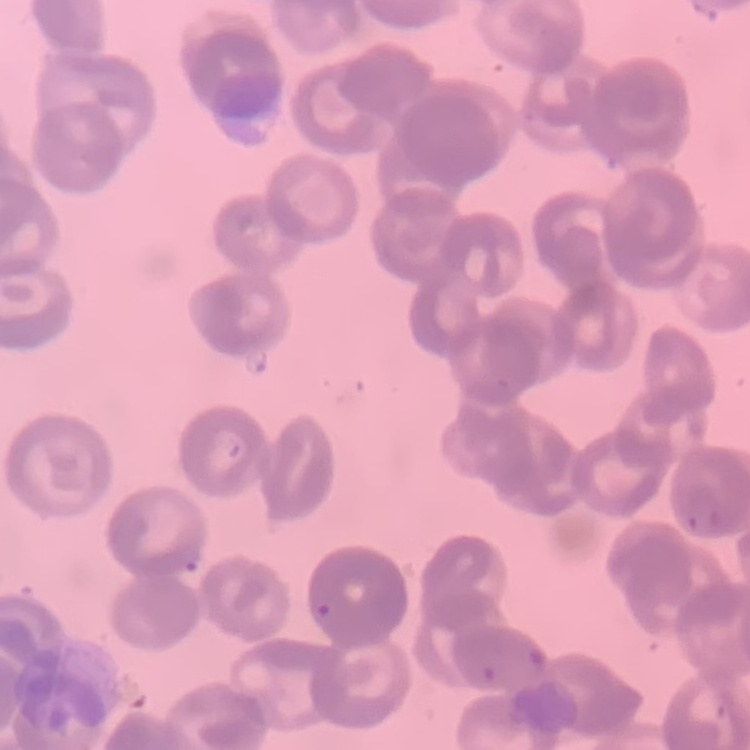

Summary:
  - Red blood cell morphology: rouleaux formation
  - Image type: square crop of a larger photomicrograph
  - Preparation: thin blood film
  - Stain: Field's or Giemsa